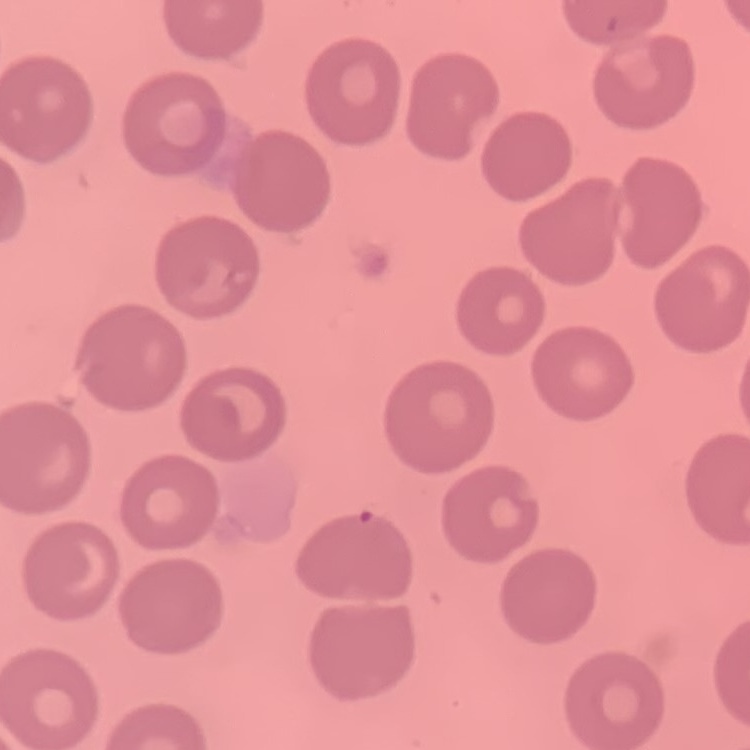

red_blood_cell_morphology: no rouleaux formation
preparation: thin blood smear
stain: Field's or Giemsa
image_type: one tile cut from a larger photomicrograph